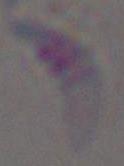 Toxoplasma gondii is seen. Captured at 1000x magnification. Photomicrograph.